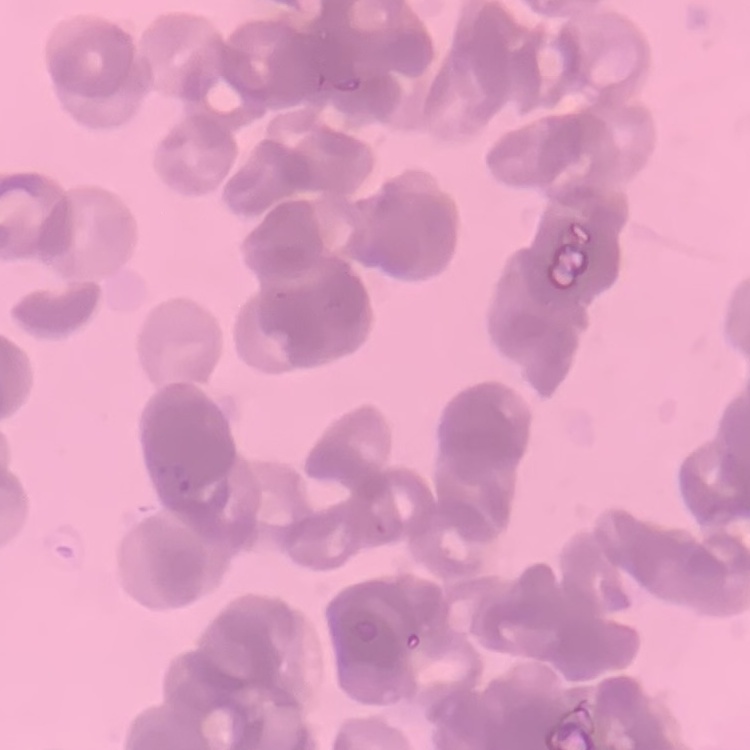
red blood cell morphology = rouleaux formation
stain = Field's or Giemsa
image type = one tile cut from a larger photomicrograph
preparation = thin blood smear